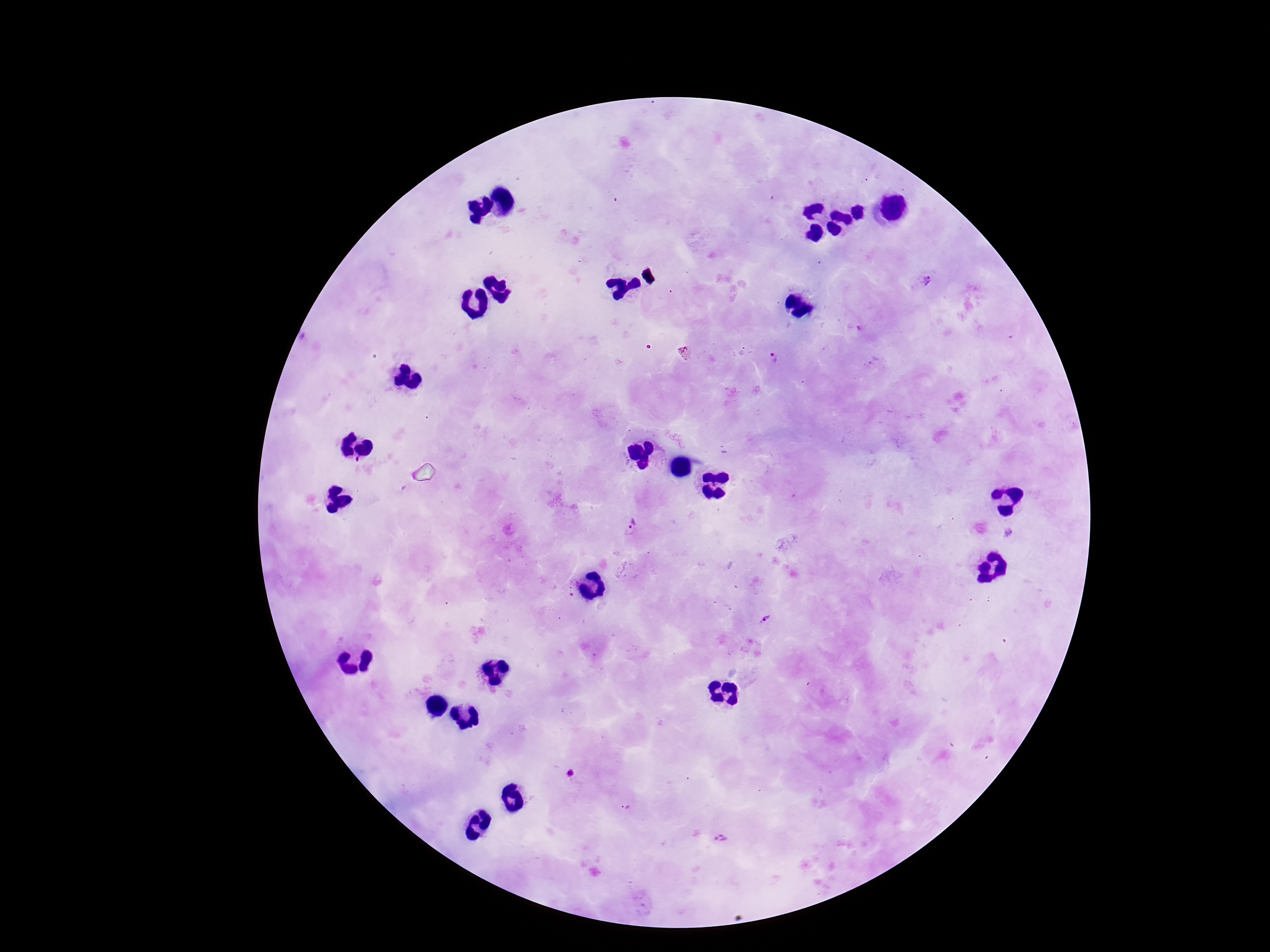
Approximate centers as {x, y} in pixels.
Summary:
  - Plasmodium parasite locations: {925, 281}, {779, 359}, {632, 527}, {765, 619}, {625, 809}, {717, 838}
  - Field of view: single
  - Image size: 1270×952 pixels
  - Preparation: thick blood film
  - Patient malaria status: infected
  - Stain: Giemsa
  - Magnification: 100x
  - Capture: smartphone camera through the microscope eyepiece